Give the position of every malaria parasite and every leukocyte.
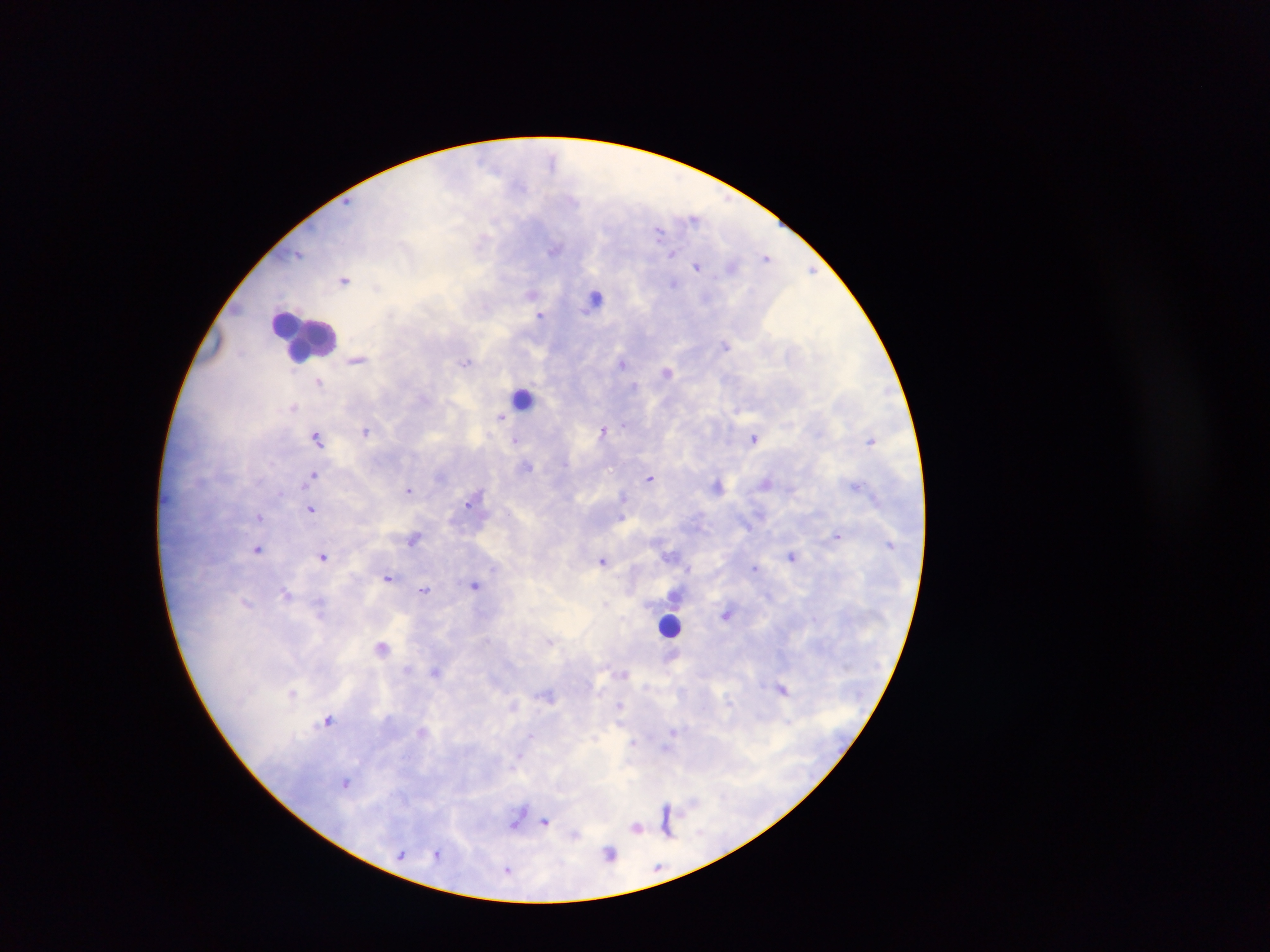
Approximate centers as (x, y) in pixels.
Malaria parasites: (552, 158), (521, 185), (695, 218), (659, 230), (556, 249), (671, 253), (298, 254), (766, 256), (698, 266), (732, 267), (812, 270), (344, 280), (674, 283), (377, 287), (531, 293), (540, 315), (726, 345), (357, 360), (466, 362), (622, 362), (666, 372), (318, 381), (634, 386), (293, 407), (501, 417), (624, 424), (603, 429), (366, 431), (317, 438), (754, 438), (515, 440), (871, 441), (528, 466), (314, 474), (440, 476), (649, 478), (766, 482), (717, 485), (857, 485), (409, 490), (623, 496), (470, 502), (311, 509), (508, 513), (259, 516), (837, 536), (414, 539), (258, 549), (672, 556), (792, 556), (323, 557), (603, 560), (755, 567), (689, 569), (388, 577), (475, 585), (425, 590), (286, 594), (606, 603), (728, 613), (551, 641), (382, 647), (435, 672), (624, 673), (782, 688), (292, 693), (547, 695), (619, 704), (514, 705), (328, 720), (672, 731), (530, 735), (595, 738), (633, 743), (666, 749), (520, 756), (346, 782), (666, 809), (517, 818), (666, 818), (546, 821), (636, 827), (666, 829), (436, 853), (402, 854), (610, 854), (508, 870).
Leukocytes: (596, 297), (304, 337), (522, 398), (669, 625).

Photographed through a microscope with a mobile-phone camera. Single field of view. Image is 1270×952 pixels. Thick blood smear. Sample from Ghana.